Identify the cell.
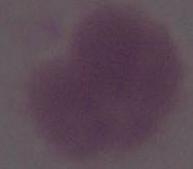

This is an erythrocyte.

modality = photomicrograph
magnification = 1000x